Locate every blood parasite and identify its species.
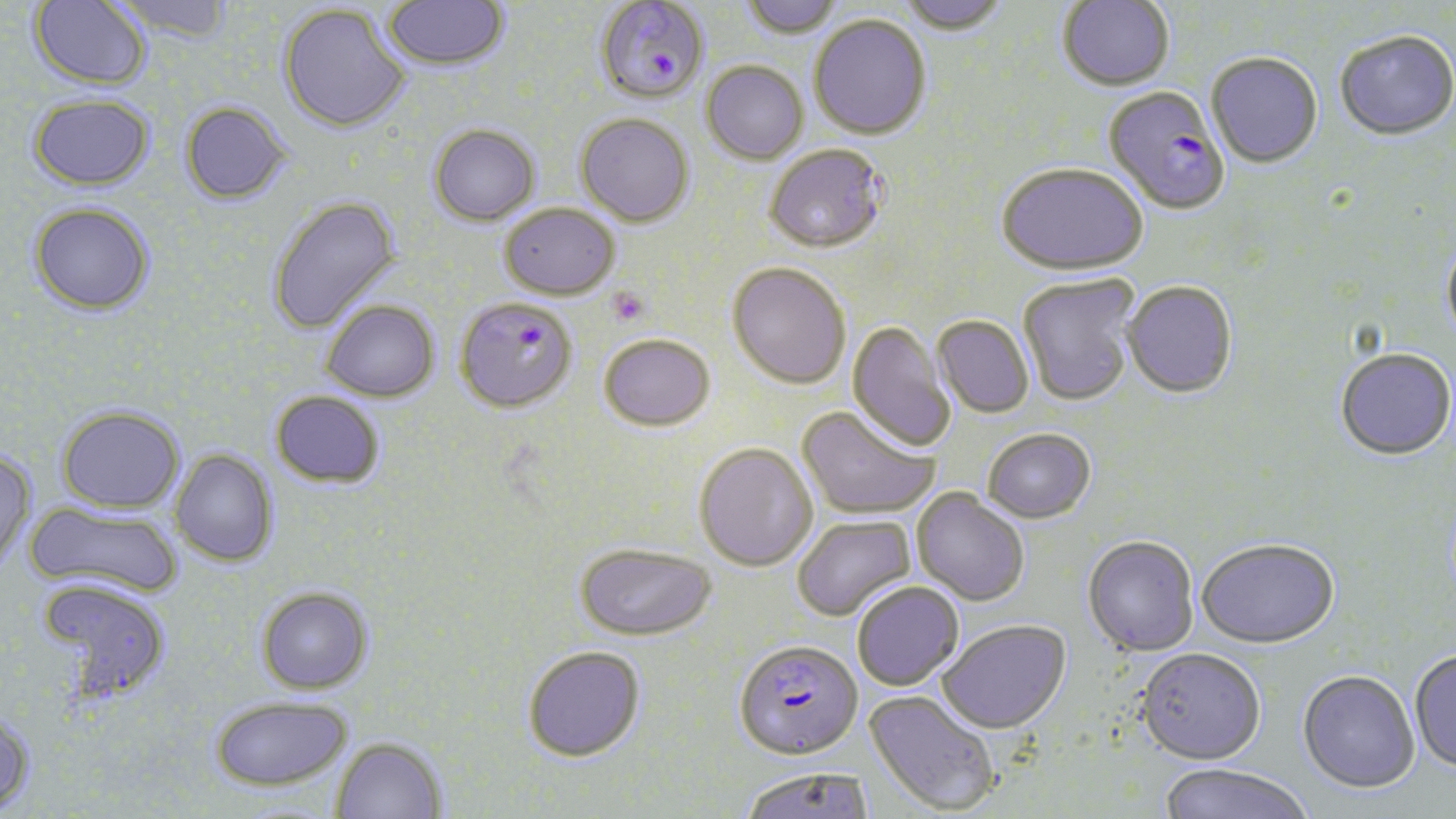

Approximate bounding boxes as [x1, y1, x2, y2] in pixels.
Plasmodium falciparum-infected red blood cells: [594, 1, 709, 105], [1104, 86, 1229, 214], [461, 305, 578, 415], [733, 637, 862, 760].
No Plasmodium ovale, Plasmodium malariae, Plasmodium vivax, Babesia divergens, or Trypanosoma brucei observed.

Platelet locations: [607, 287, 650, 326]. Uninfected red blood cell locations: [29, 0, 151, 89], [110, 0, 235, 44], [740, 0, 845, 39], [896, 0, 1009, 34], [1058, 0, 1174, 90], [383, 1, 510, 72], [278, 3, 411, 133], [809, 14, 931, 139], [1335, 28, 1456, 139], [1206, 52, 1322, 168], [701, 61, 808, 164], [28, 92, 155, 190], [180, 101, 292, 205], [576, 113, 694, 226], [429, 124, 540, 225], [764, 144, 888, 254], [997, 163, 1147, 276], [267, 194, 401, 335], [28, 201, 156, 316], [499, 203, 620, 300], [1441, 236, 1456, 347], [728, 262, 852, 389], [1017, 273, 1140, 407], [1123, 280, 1238, 398], [321, 299, 440, 402], [933, 315, 1034, 417], [847, 320, 955, 453], [598, 333, 715, 431], [1335, 347, 1456, 460], [270, 391, 385, 489], [56, 405, 186, 513], [797, 405, 940, 520], [982, 427, 1096, 522], [694, 442, 818, 571], [170, 449, 278, 567], [0, 450, 37, 572], [913, 488, 1030, 605], [25, 500, 184, 600], [792, 515, 916, 622], [1082, 534, 1199, 656], [1196, 536, 1340, 648], [575, 542, 717, 640], [35, 578, 172, 704], [852, 581, 964, 690], [256, 585, 373, 694], [937, 619, 1071, 733], [523, 645, 645, 762], [1136, 647, 1266, 764], [1409, 648, 1456, 774], [1297, 669, 1420, 793], [865, 689, 1002, 816], [209, 695, 353, 790], [0, 711, 37, 817], [331, 737, 447, 819], [1157, 763, 1314, 819], [739, 766, 874, 819]. Slide-level diagnosis: Plasmodium falciparum. Thin blood film. One field of a larger specimen. Optical microscopy. Image is 1456×819 pixels. Captured at 1000x magnification. May-Grünwald-Giemsa stain.